Name the parasite shown.
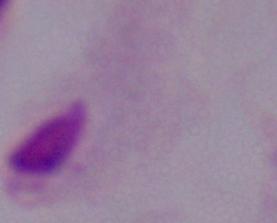

This is a trichomonad.

Summary:
  - Magnification: 1000x
  - Modality: micrograph